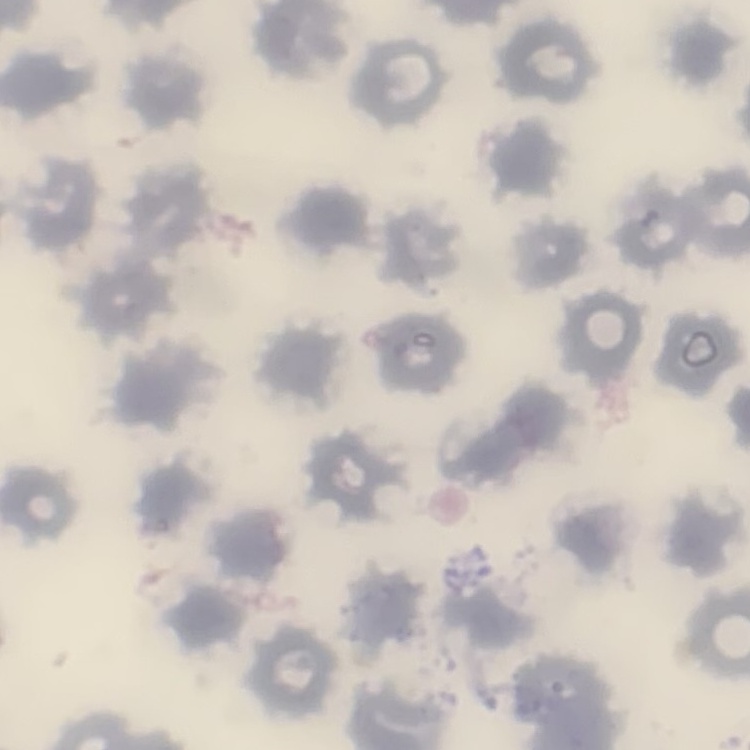
erythrocyte morphology = no rouleaux formation
stain = Field's or Giemsa
image type = one tile cut from a larger photomicrograph
preparation = thin blood film